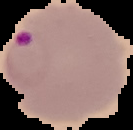 Segmented cell region on a black background. Image is 133×130 pixels. From a thin blood smear. Result: malaria parasites detected.